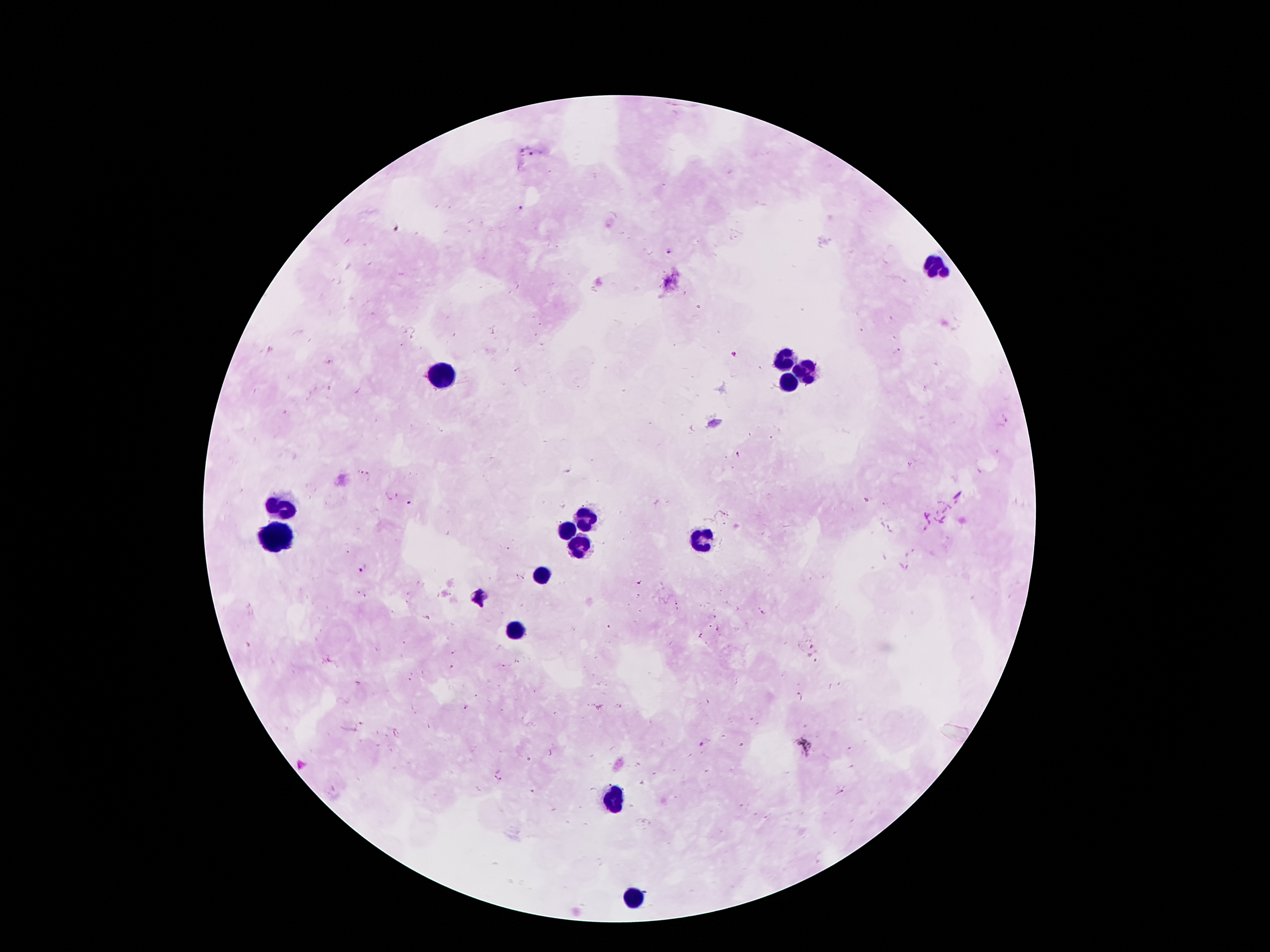
Approximate centers as {x, y} in pixels. Plasmodium parasite locations: {531, 153}, {522, 208}, {667, 251}, {898, 351}, {735, 353}, {517, 371}, {410, 503}, {363, 569}, {640, 582}, {639, 597}, {478, 599}, {677, 602}, {762, 613}, {713, 616}, {709, 626}, {719, 629}, {700, 636}, {452, 666}, {798, 693}, {468, 707}, {750, 719}, {701, 744}, {842, 791}. Leukocyte locations: {938, 270}, {785, 360}, {806, 371}, {440, 379}, {787, 381}, {287, 507}, {587, 516}, {570, 528}, {277, 537}, {705, 539}, {579, 543}, {541, 574}, {516, 631}, {613, 801}, {636, 900}. 100x magnification. Image is 1270×952 pixels. Smartphone photograph taken through the microscope eyepiece. Giemsa-stained preparation. Single field of view. Thick blood smear. Patient malaria status: positive for Plasmodium falciparum.